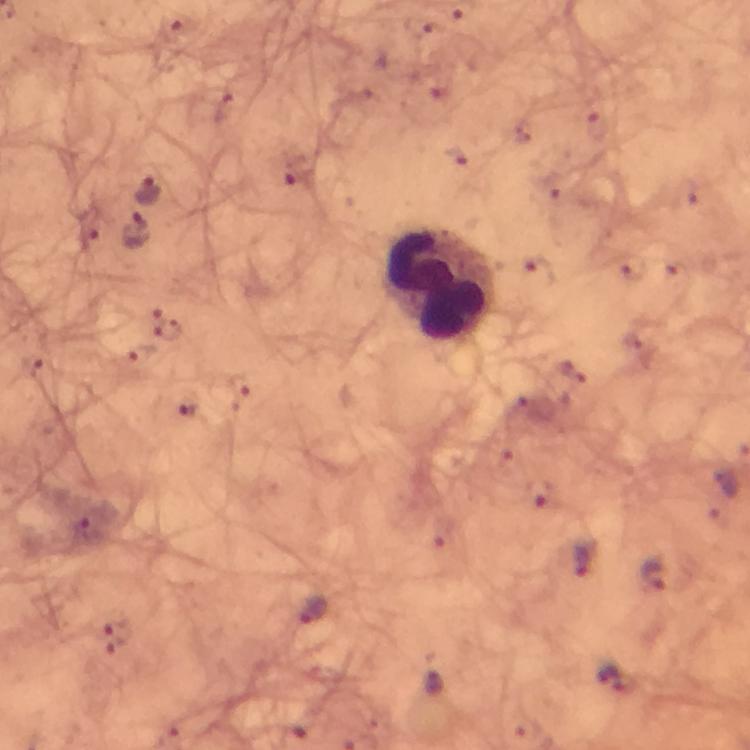

context: from a diagnostic examination for malaria
immersion_oil: applied
cropped_from: a single field of view
malaria_parasite_locations: 'approximate centers as {x, y} in pixels: {147, 191}, {138, 230}, {170, 330}, {131, 359}, {32, 367}, {190, 409}, {726, 483}, {87, 529}, {586, 560}, {653, 576}, {313, 610}, {118, 639}, {435, 681}, {623, 682}'
capture: smartphone camera through the microscope
stain: Giemsa
magnification: 100x
leukocyte_locations: 'approximate centers as {x, y} in pixels: {443, 285}'
preparation: thick blood smear
image_size: 750×750 pixels